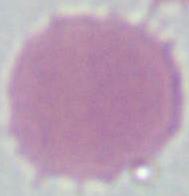

{
  "modality": "photomicrograph",
  "identification": "erythrocyte",
  "magnification": "1000x"
}